State which parasite is depicted.
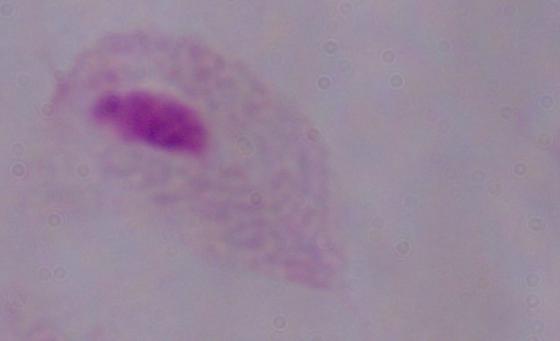

This is a trichomonad.

Captured at 1000x magnification. Photomicrograph.